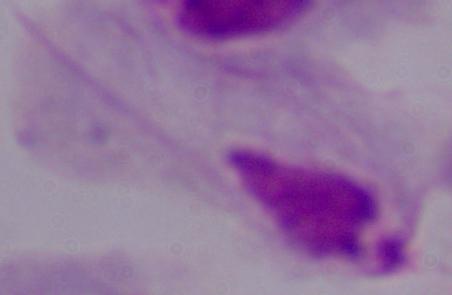

magnification = 1000x
identification = trichomonad
modality = photomicrograph